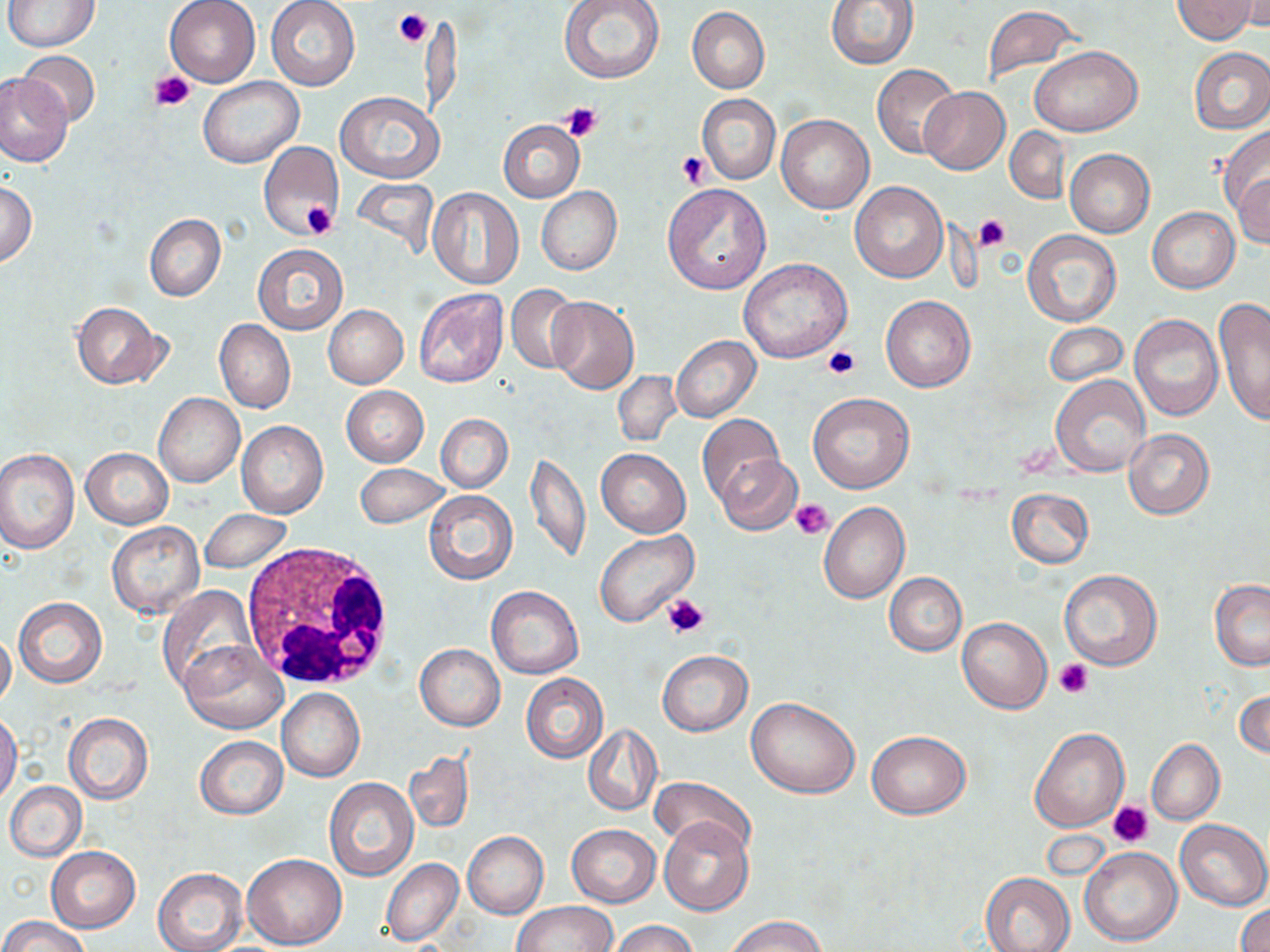 Approximate bounding boxes as [x1, y1, x2, y2] in pixels. Platelet locations: [393, 10, 433, 50], [152, 71, 197, 111], [561, 101, 602, 141], [678, 152, 710, 187], [301, 201, 338, 239], [974, 214, 1010, 251], [821, 346, 860, 379], [790, 498, 834, 538], [664, 592, 711, 638], [1054, 659, 1094, 698], [1109, 800, 1154, 846]. White blood cell locations: [240, 543, 394, 690]. Uninfected red blood cell locations: [3, 0, 100, 51], [164, 0, 261, 87], [266, 0, 359, 90], [559, 0, 666, 84], [827, 0, 919, 68], [1174, 0, 1256, 43], [1230, 2, 1270, 34], [983, 5, 1082, 83], [687, 7, 769, 94], [1031, 45, 1140, 136], [1189, 47, 1270, 133], [16, 51, 101, 126], [871, 63, 959, 158], [1, 75, 72, 166], [198, 77, 302, 168], [919, 86, 1010, 175], [335, 91, 442, 184], [697, 93, 781, 184], [776, 114, 873, 213], [498, 119, 585, 203], [1005, 126, 1070, 204], [1219, 128, 1270, 228], [258, 141, 343, 240], [1065, 148, 1155, 238], [1232, 169, 1270, 249], [350, 179, 439, 258], [849, 181, 947, 283], [0, 182, 38, 266], [662, 183, 771, 293], [535, 185, 622, 275], [428, 187, 523, 289], [1149, 207, 1239, 294], [144, 214, 226, 303], [1022, 229, 1122, 327], [253, 243, 346, 335], [738, 257, 853, 363], [506, 283, 582, 375], [413, 288, 510, 389], [880, 295, 975, 392], [546, 296, 639, 394], [1214, 297, 1270, 422], [71, 301, 168, 389], [324, 305, 408, 388], [1130, 313, 1223, 421], [215, 320, 295, 413], [1043, 322, 1126, 385], [672, 336, 761, 422], [613, 372, 682, 448], [1051, 374, 1151, 476], [341, 385, 429, 467], [807, 392, 916, 493], [153, 393, 244, 487], [436, 414, 512, 493], [697, 414, 784, 505], [236, 422, 328, 519], [1123, 429, 1214, 519], [82, 447, 173, 529], [595, 448, 690, 538], [0, 449, 80, 553], [526, 452, 590, 564], [717, 454, 802, 536], [354, 463, 451, 529], [1006, 488, 1093, 568], [423, 490, 517, 584], [818, 502, 909, 603], [199, 509, 294, 573], [106, 521, 205, 618], [595, 530, 697, 627], [1059, 569, 1162, 670], [885, 571, 967, 656], [1209, 580, 1270, 670], [486, 585, 583, 679], [157, 586, 259, 695], [14, 597, 106, 688], [957, 618, 1052, 714], [0, 629, 16, 709], [179, 640, 286, 733], [415, 644, 505, 730], [657, 650, 753, 736], [521, 674, 609, 763], [1235, 687, 1269, 762], [277, 688, 364, 782], [746, 697, 860, 800], [0, 713, 22, 805], [63, 714, 153, 803], [583, 723, 661, 816], [1030, 728, 1128, 832], [866, 730, 970, 818], [195, 736, 287, 819], [1146, 739, 1223, 825], [404, 751, 474, 833], [649, 775, 755, 857], [324, 778, 418, 882], [4, 782, 86, 861], [658, 817, 753, 915], [1175, 819, 1269, 911], [566, 823, 661, 907], [463, 832, 547, 918], [1079, 846, 1183, 946], [47, 847, 140, 933], [241, 853, 348, 949], [380, 858, 463, 945], [153, 867, 247, 952], [981, 873, 1075, 952], [514, 901, 617, 951], [1235, 902, 1270, 952], [725, 914, 827, 952], [0, 915, 91, 952], [610, 920, 698, 952]. Slide-level diagnosis: no evidence of blood parasites. May-Grünwald-Giemsa-stained preparation. Single field of view. 1000x magnification. Optical microscopy. Image is 1270×952 pixels. Thin blood film.